Classify this cell by malaria status.
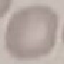

Uninfected.

{
  "stain": "Giemsa",
  "image_type": "cell patch, automatically extracted from a larger field of view and resized to 64 × 64 pixels",
  "capture": "smartphone through the microscope eyepiece",
  "preparation": "thin smear"
}